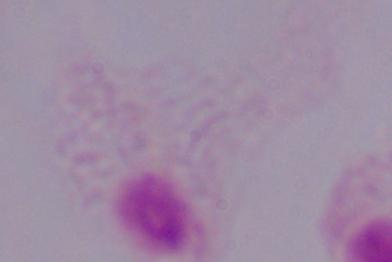

magnification = 1000x
modality = photomicrograph
identification = trichomonad